Assess for Plasmodium parasites.
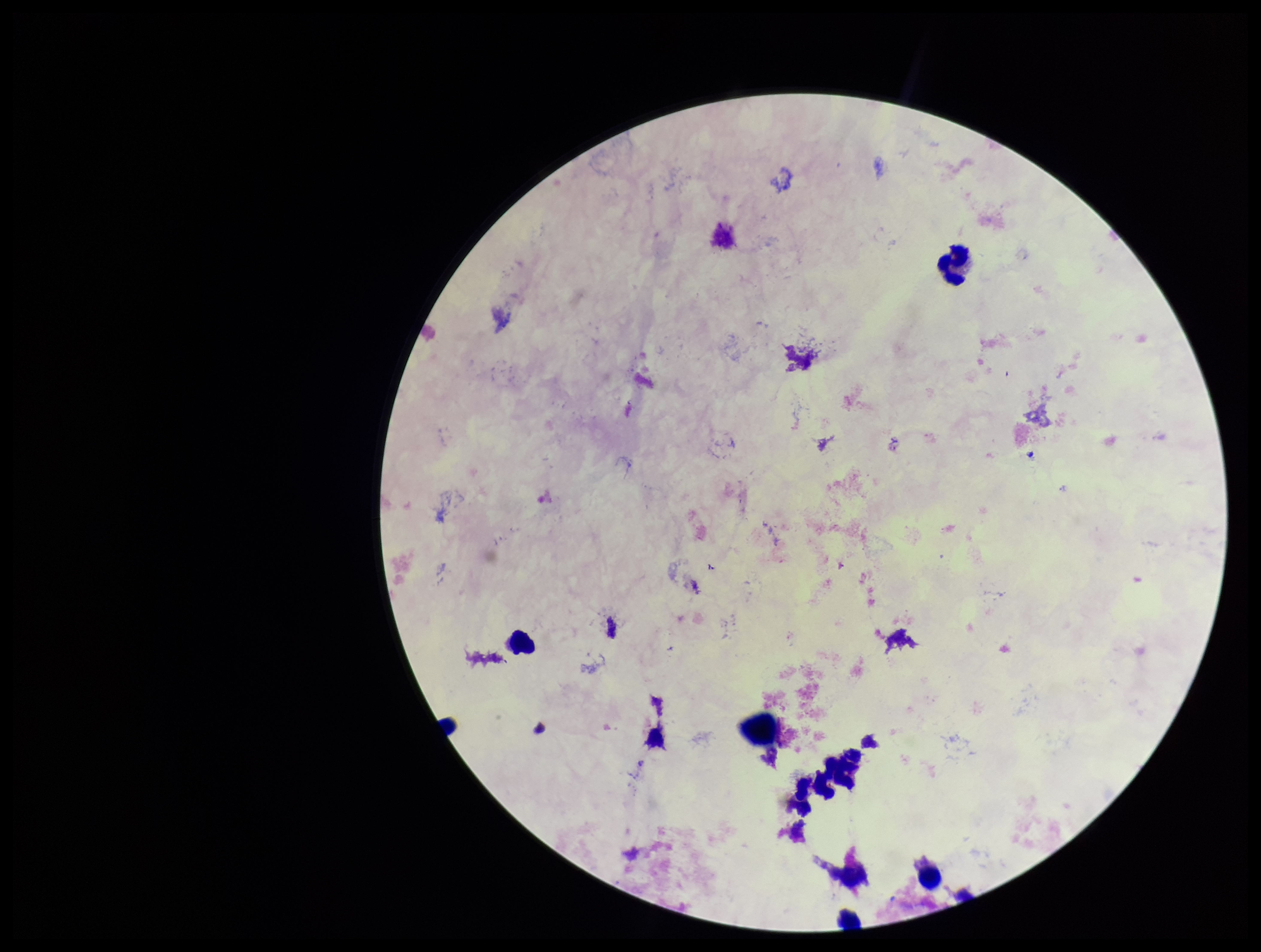
None identified.

Giemsa stain. Patient malaria status: negative. Single field of view. Parasite count: 0. Image is 1261×952 pixels. Leukocyte count: 7. Photographed through the microscope eyepiece with a smartphone camera. Preparation: thick smear.